Locate every blood parasite and identify its species.
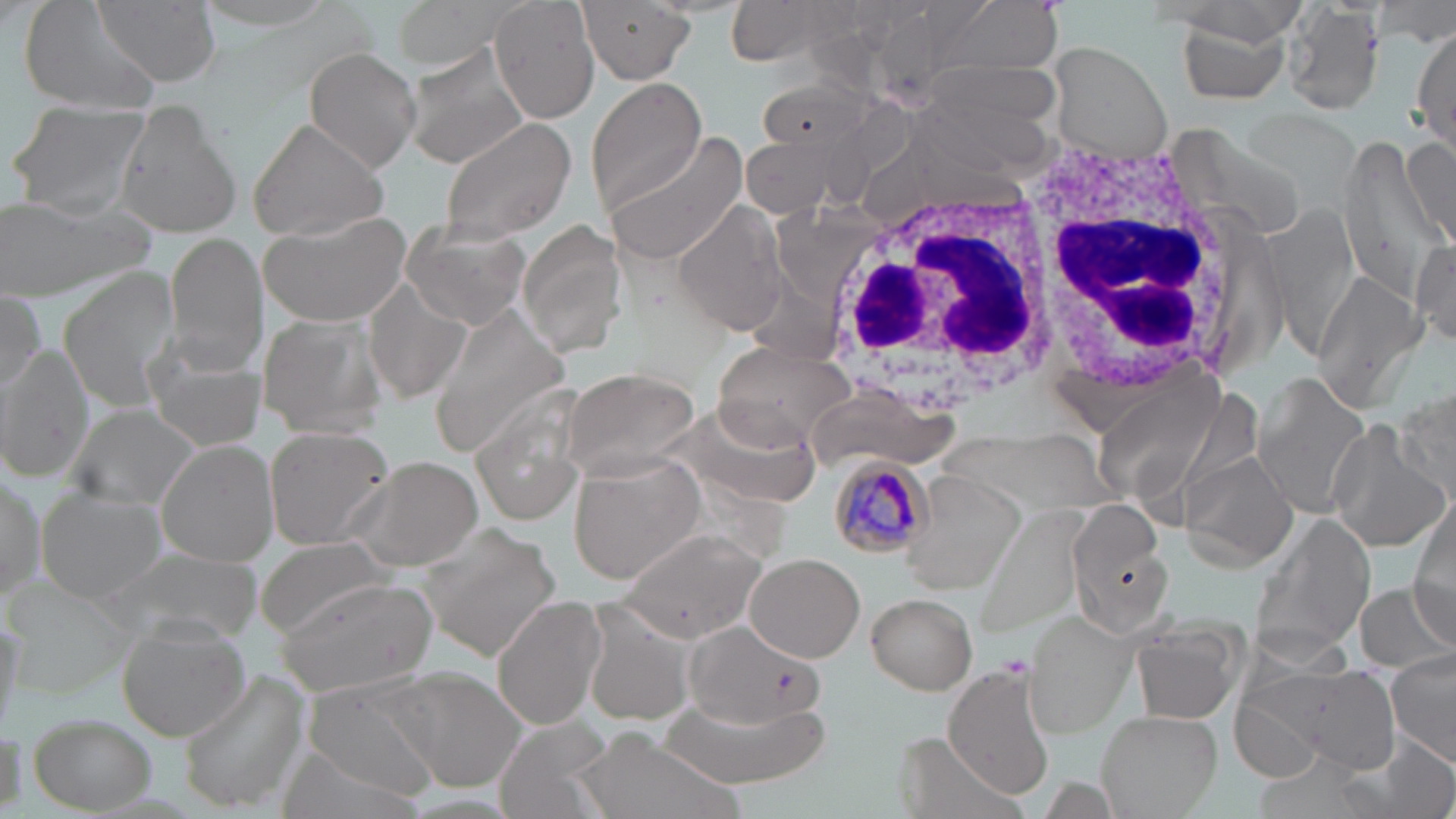
Approximate bounding boxes as named x1/y1/x2/y2 corners in pixels.
Plasmodium malariae-infected red blood cells: (x1=830, y1=458, x2=939, y2=561).
No Plasmodium falciparum, Plasmodium ovale, Plasmodium vivax, Babesia divergens, or Trypanosoma brucei observed.

{
  "slide_level_diagnosis": "Plasmodium malariae",
  "field_of_view": "single",
  "modality": "optical microscopy",
  "white_blood_cell_locations": "approximate bounding boxes as named x1/y1/x2/y2 corners in pixels: (x1=1007, y1=129, x2=1250, y2=400), (x1=824, y1=182, x2=1055, y2=408)",
  "uninfected_red_blood_cell_locations": "approximate bounding boxes as named x1/y1/x2/y2 corners in pixels: (x1=18, y1=0, x2=165, y2=112), (x1=190, y1=0, x2=355, y2=39), (x1=388, y1=0, x2=521, y2=70), (x1=489, y1=0, x2=601, y2=124), (x1=723, y1=0, x2=851, y2=67), (x1=934, y1=0, x2=1067, y2=76), (x1=90, y1=1, x2=220, y2=87), (x1=576, y1=1, x2=695, y2=86), (x1=1281, y1=3, x2=1388, y2=115), (x1=1172, y1=9, x2=1299, y2=106), (x1=1410, y1=27, x2=1456, y2=155), (x1=400, y1=42, x2=530, y2=170), (x1=1046, y1=43, x2=1175, y2=160), (x1=304, y1=47, x2=422, y2=173), (x1=915, y1=56, x2=1067, y2=139), (x1=756, y1=76, x2=876, y2=153), (x1=590, y1=78, x2=707, y2=216), (x1=900, y1=95, x2=1053, y2=182), (x1=10, y1=102, x2=154, y2=221), (x1=111, y1=103, x2=242, y2=239), (x1=1243, y1=109, x2=1360, y2=209), (x1=247, y1=115, x2=391, y2=245), (x1=439, y1=116, x2=578, y2=245), (x1=1170, y1=127, x2=1311, y2=243), (x1=609, y1=131, x2=753, y2=266), (x1=1332, y1=135, x2=1453, y2=304), (x1=1402, y1=137, x2=1456, y2=255), (x1=744, y1=138, x2=835, y2=216), (x1=1, y1=197, x2=151, y2=297), (x1=673, y1=199, x2=792, y2=336), (x1=1260, y1=201, x2=1359, y2=361), (x1=259, y1=206, x2=414, y2=327), (x1=401, y1=219, x2=531, y2=331), (x1=518, y1=220, x2=620, y2=359), (x1=163, y1=233, x2=268, y2=374), (x1=1412, y1=235, x2=1456, y2=346), (x1=58, y1=264, x2=179, y2=407), (x1=1310, y1=270, x2=1427, y2=413), (x1=364, y1=279, x2=472, y2=405), (x1=0, y1=292, x2=46, y2=396), (x1=429, y1=307, x2=572, y2=451), (x1=257, y1=312, x2=388, y2=439), (x1=713, y1=338, x2=857, y2=451), (x1=0, y1=344, x2=94, y2=482), (x1=146, y1=353, x2=266, y2=451), (x1=560, y1=365, x2=702, y2=479), (x1=1250, y1=372, x2=1376, y2=517), (x1=1093, y1=376, x2=1224, y2=506), (x1=1392, y1=383, x2=1454, y2=509), (x1=675, y1=393, x2=825, y2=509), (x1=466, y1=403, x2=591, y2=524), (x1=68, y1=405, x2=203, y2=513), (x1=1326, y1=422, x2=1453, y2=552), (x1=262, y1=424, x2=395, y2=551), (x1=156, y1=440, x2=280, y2=567), (x1=1179, y1=450, x2=1298, y2=571), (x1=343, y1=454, x2=486, y2=572), (x1=567, y1=454, x2=705, y2=586), (x1=897, y1=468, x2=1026, y2=593), (x1=0, y1=471, x2=48, y2=604), (x1=36, y1=487, x2=164, y2=602), (x1=1409, y1=497, x2=1456, y2=632), (x1=1069, y1=501, x2=1167, y2=623), (x1=976, y1=506, x2=1086, y2=634), (x1=1255, y1=513, x2=1377, y2=653), (x1=618, y1=525, x2=765, y2=638), (x1=426, y1=531, x2=560, y2=660), (x1=255, y1=539, x2=391, y2=636), (x1=104, y1=547, x2=264, y2=643), (x1=746, y1=553, x2=865, y2=662), (x1=277, y1=577, x2=437, y2=695), (x1=1357, y1=583, x2=1452, y2=671), (x1=864, y1=592, x2=977, y2=695), (x1=493, y1=596, x2=608, y2=731), (x1=581, y1=607, x2=695, y2=728), (x1=0, y1=613, x2=27, y2=732), (x1=1019, y1=613, x2=1142, y2=737), (x1=118, y1=622, x2=250, y2=740), (x1=685, y1=622, x2=822, y2=731), (x1=1132, y1=623, x2=1246, y2=727), (x1=1387, y1=662, x2=1456, y2=767), (x1=943, y1=665, x2=1054, y2=800), (x1=1264, y1=667, x2=1404, y2=776), (x1=181, y1=669, x2=311, y2=813), (x1=394, y1=670, x2=529, y2=791), (x1=1230, y1=683, x2=1347, y2=786), (x1=301, y1=687, x2=441, y2=802), (x1=662, y1=697, x2=825, y2=786), (x1=1097, y1=708, x2=1223, y2=818), (x1=29, y1=712, x2=155, y2=814), (x1=498, y1=715, x2=614, y2=818), (x1=567, y1=728, x2=729, y2=819), (x1=1345, y1=735, x2=1456, y2=819), (x1=278, y1=746, x2=429, y2=819)",
  "preparation": "thin blood film",
  "image_size": "1456×819 pixels",
  "magnification": "1000x",
  "stain": "May-Grünwald-Giemsa"
}